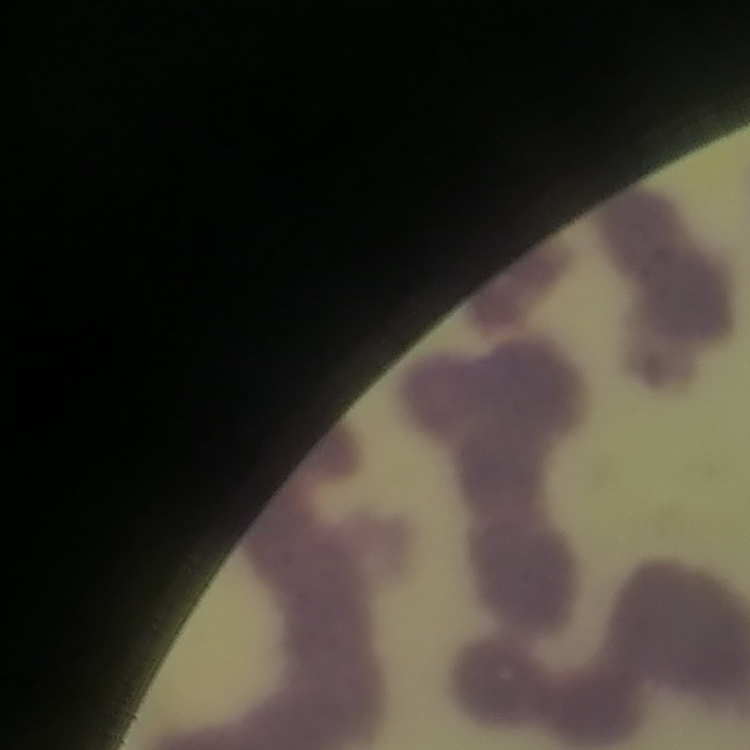

{
  "erythrocyte_morphology": "rouleaux formation",
  "image_type": "square crop of a larger photomicrograph",
  "stain": "Field's or Giemsa",
  "preparation": "thin blood film"
}